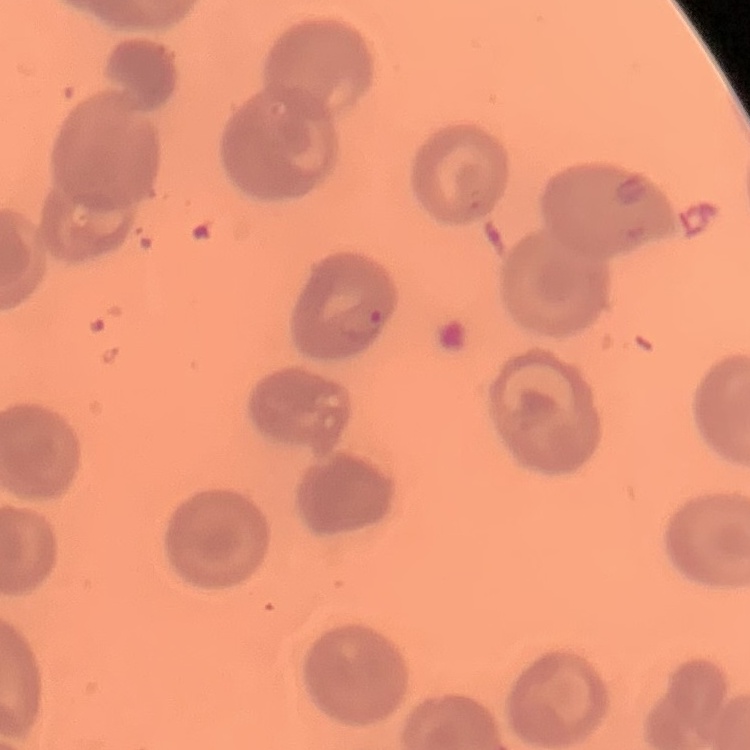

red blood cell morphology = no rouleaux formation
preparation = thin blood smear
image type = square crop of a larger photomicrograph
stain = Field's or Giemsa